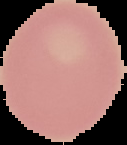

Summary:
  - Image type: cell region segmented out of the field of view; surrounding area masked to black
  - Preparation: thin blood smear
  - Image size: 127×145 pixels
  - Result: negative for Plasmodium parasites